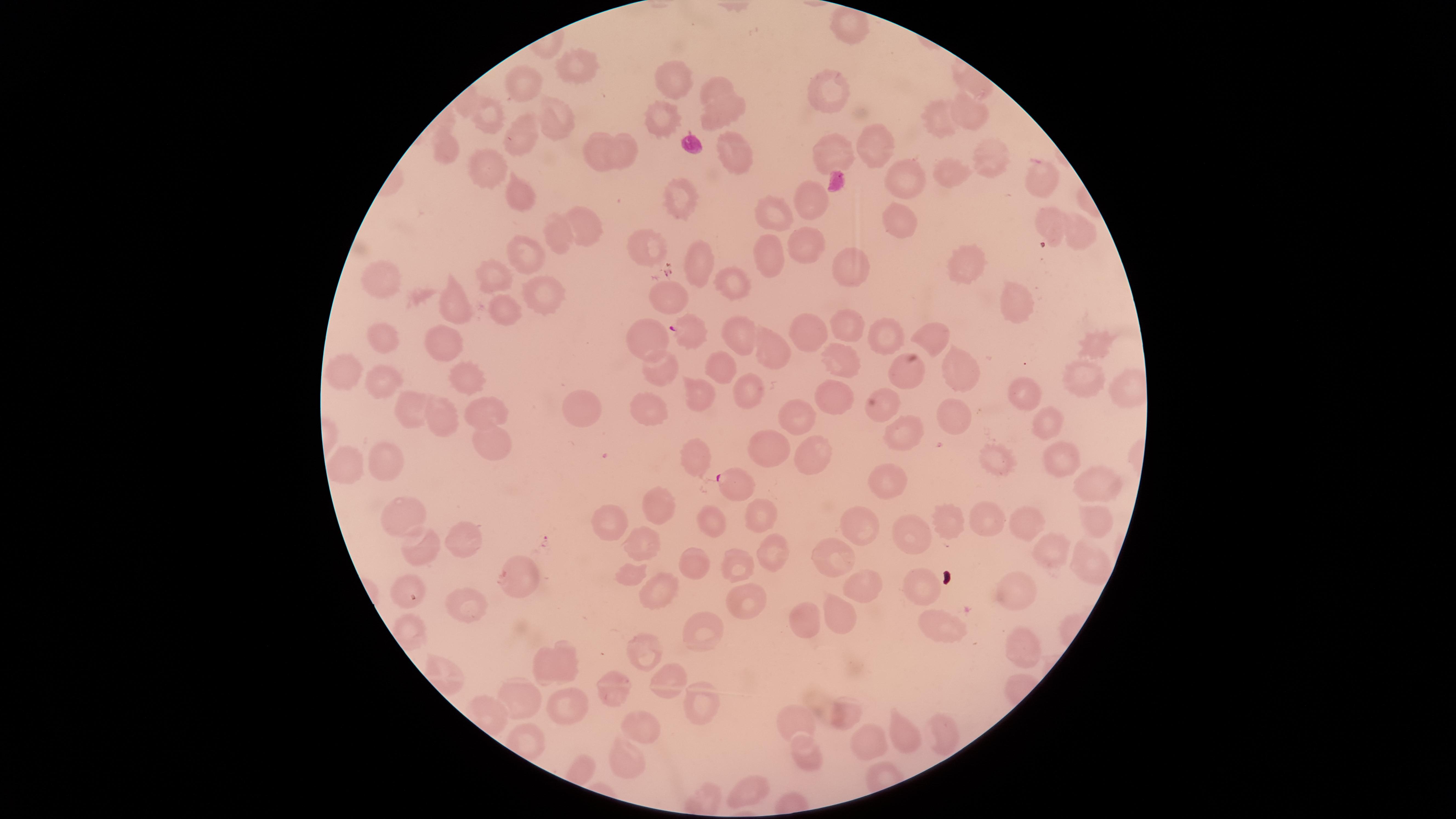

uninfected_red_blood_cells: 'approximate marker points, in pixels from the top-left corner: (x=845, y=22), (x=570, y=65), (x=526, y=81), (x=670, y=81), (x=717, y=86), (x=831, y=91), (x=488, y=110), (x=722, y=110), (x=973, y=112), (x=657, y=116), (x=930, y=118), (x=552, y=120), (x=521, y=135), (x=879, y=140), (x=735, y=146), (x=622, y=147), (x=444, y=150), (x=596, y=151), (x=988, y=155), (x=839, y=157), (x=483, y=169), (x=911, y=173), (x=954, y=176), (x=1043, y=179), (x=514, y=191), (x=687, y=196), (x=809, y=204), (x=777, y=211), (x=903, y=214), (x=581, y=223), (x=1051, y=223), (x=1072, y=228), (x=556, y=236), (x=802, y=241), (x=644, y=246), (x=523, y=252), (x=762, y=252), (x=693, y=256), (x=846, y=262), (x=967, y=266), (x=494, y=276), (x=386, y=280), (x=738, y=283), (x=538, y=290), (x=671, y=292), (x=1013, y=298), (x=450, y=302), (x=500, y=309), (x=860, y=326), (x=883, y=326), (x=813, y=331), (x=937, y=333), (x=653, y=336), (x=383, y=338), (x=739, y=338), (x=444, y=340), (x=778, y=344), (x=1097, y=344), (x=844, y=358), (x=351, y=364), (x=721, y=365), (x=663, y=368), (x=905, y=370), (x=961, y=373), (x=469, y=375), (x=1083, y=375), (x=375, y=381), (x=702, y=386), (x=1024, y=389), (x=753, y=390), (x=830, y=395), (x=655, y=398), (x=483, y=405), (x=576, y=408), (x=407, y=410), (x=887, y=410), (x=962, y=414), (x=803, y=415), (x=447, y=417), (x=1051, y=423), (x=490, y=436), (x=905, y=436), (x=765, y=444), (x=812, y=454), (x=699, y=456), (x=1002, y=456), (x=384, y=459), (x=1053, y=460), (x=345, y=467), (x=881, y=483), (x=1093, y=489), (x=662, y=504), (x=981, y=513), (x=396, y=515), (x=753, y=516), (x=949, y=516), (x=616, y=518), (x=1025, y=518), (x=1085, y=518), (x=708, y=520), (x=868, y=522), (x=903, y=532), (x=465, y=537), (x=770, y=544), (x=640, y=547), (x=1051, y=547), (x=838, y=551), (x=432, y=553), (x=1082, y=559), (x=680, y=562), (x=738, y=570), (x=633, y=573), (x=517, y=574), (x=866, y=588), (x=1010, y=588), (x=407, y=591), (x=655, y=591), (x=917, y=591), (x=750, y=600), (x=465, y=607), (x=811, y=616), (x=835, y=616), (x=943, y=621), (x=700, y=636), (x=1015, y=642), (x=642, y=649), (x=556, y=656), (x=671, y=676), (x=621, y=689), (x=699, y=695), (x=515, y=696), (x=575, y=701), (x=842, y=711), (x=802, y=717), (x=643, y=724), (x=941, y=730), (x=907, y=733), (x=873, y=738), (x=806, y=748), (x=622, y=753), (x=750, y=784)'
presence: malaria parasites seen
capture: smartphone photograph through the microscope eyepiece
field_of_view: single
image_size: 1456×819 pixels
parasitized_red_blood_cells: 'approximate marker points, in pixels from the top-left corner: (x=687, y=330), (x=732, y=483)'
stain: Giemsa
preparation: thin blood smear
species: Plasmodium falciparum
visible_region: circular